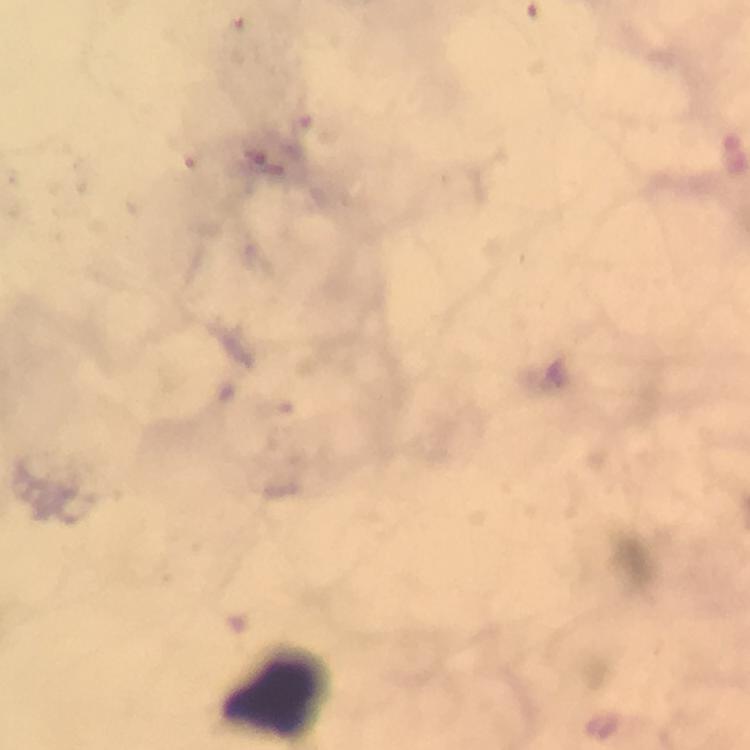
Approximate centers as (x, y) in pixels.
Summary:
  - Plasmodium parasite locations: (267, 164)
  - Leukocyte locations: (272, 697)
  - Image size: 750×750 pixels
  - Capture: smartphone photograph through a microscope
  - Context: from a diagnostic examination for malaria
  - Stain: Giemsa
  - Cropped from: one field of view
  - Immersion oil: used
  - Magnification: 100x
  - Preparation: thick blood smear